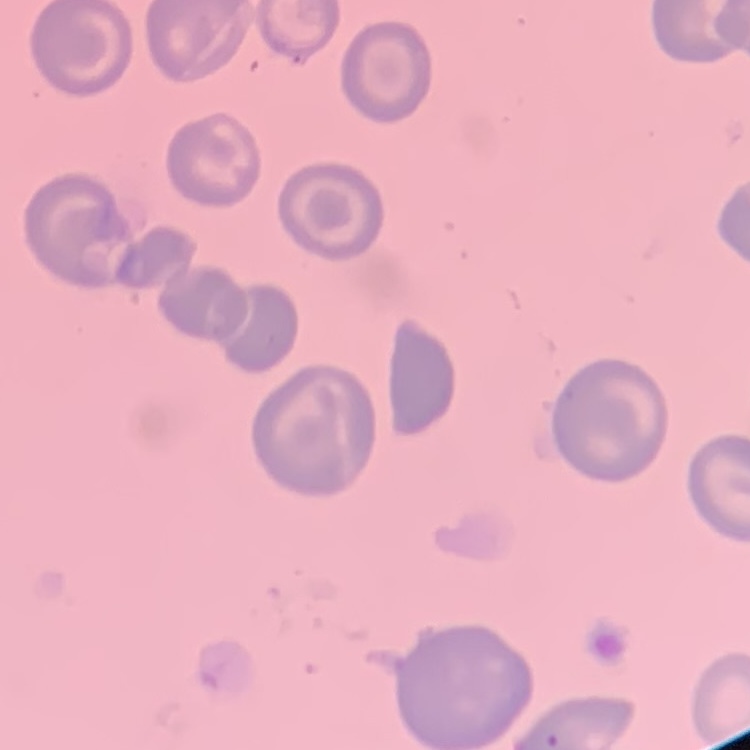

erythrocyte_morphology: no rouleaux formation
stain: Field's or Giemsa
image_type: square crop of a larger photomicrograph
preparation: thin blood film